Give the extent of all uninfected red blood cells.
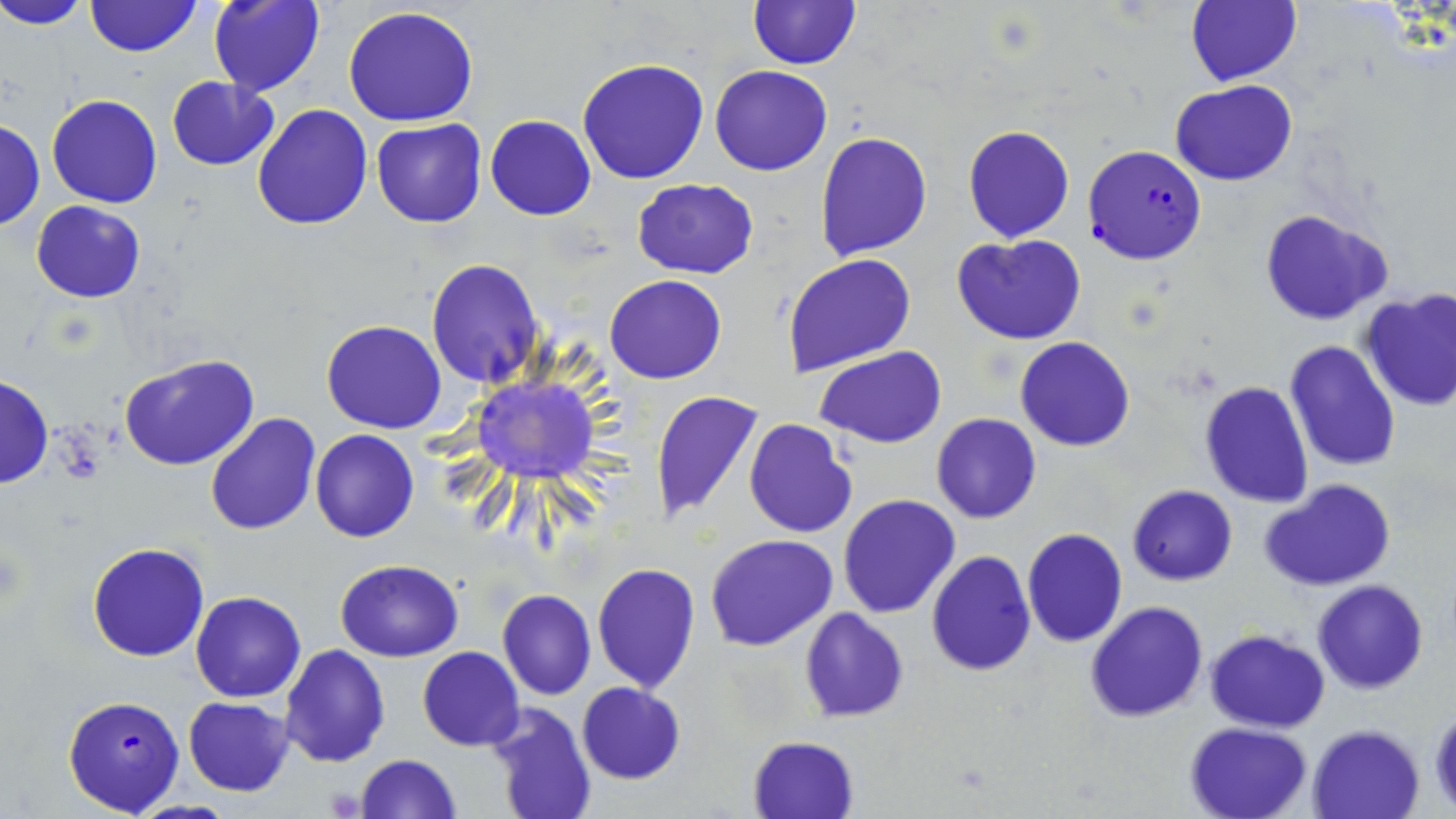

Approximate bounding boxes as named x1/y1/x2/y2 corners in pixels.
Uninfected red blood cells: (x1=0, y1=0, x2=91, y2=30), (x1=86, y1=0, x2=200, y2=56), (x1=208, y1=0, x2=325, y2=97), (x1=748, y1=0, x2=862, y2=70), (x1=1186, y1=0, x2=1301, y2=85), (x1=341, y1=7, x2=480, y2=128), (x1=576, y1=58, x2=709, y2=184), (x1=711, y1=65, x2=833, y2=176), (x1=167, y1=75, x2=279, y2=170), (x1=1170, y1=80, x2=1298, y2=184), (x1=47, y1=94, x2=161, y2=207), (x1=251, y1=102, x2=375, y2=230), (x1=485, y1=115, x2=597, y2=221), (x1=371, y1=118, x2=487, y2=227), (x1=0, y1=120, x2=45, y2=231), (x1=963, y1=125, x2=1074, y2=243), (x1=815, y1=130, x2=932, y2=261), (x1=632, y1=177, x2=759, y2=279), (x1=31, y1=200, x2=146, y2=302), (x1=1259, y1=208, x2=1392, y2=325), (x1=952, y1=233, x2=1087, y2=346), (x1=782, y1=253, x2=916, y2=376), (x1=425, y1=259, x2=544, y2=388), (x1=604, y1=274, x2=726, y2=384), (x1=1361, y1=288, x2=1456, y2=412), (x1=320, y1=319, x2=447, y2=433), (x1=1015, y1=336, x2=1135, y2=451), (x1=1284, y1=340, x2=1400, y2=470), (x1=816, y1=347, x2=947, y2=449), (x1=118, y1=354, x2=263, y2=473), (x1=1218, y1=369, x2=1399, y2=497), (x1=0, y1=375, x2=53, y2=489), (x1=472, y1=377, x2=599, y2=482), (x1=1198, y1=381, x2=1314, y2=509), (x1=651, y1=389, x2=765, y2=526), (x1=204, y1=414, x2=320, y2=535), (x1=931, y1=414, x2=1040, y2=523), (x1=743, y1=417, x2=858, y2=540), (x1=311, y1=429, x2=419, y2=542), (x1=1261, y1=479, x2=1396, y2=592), (x1=1128, y1=484, x2=1237, y2=585), (x1=837, y1=494, x2=960, y2=618), (x1=1021, y1=528, x2=1128, y2=648), (x1=706, y1=534, x2=839, y2=652), (x1=87, y1=542, x2=210, y2=662), (x1=925, y1=550, x2=1036, y2=676), (x1=334, y1=558, x2=464, y2=661), (x1=591, y1=562, x2=700, y2=693), (x1=1312, y1=579, x2=1429, y2=694), (x1=496, y1=589, x2=597, y2=699), (x1=191, y1=590, x2=306, y2=702), (x1=1085, y1=602, x2=1208, y2=722), (x1=798, y1=607, x2=909, y2=721), (x1=1205, y1=629, x2=1330, y2=731), (x1=280, y1=645, x2=391, y2=767), (x1=417, y1=646, x2=524, y2=749), (x1=576, y1=683, x2=685, y2=783), (x1=183, y1=696, x2=295, y2=795), (x1=485, y1=701, x2=597, y2=819), (x1=1429, y1=708, x2=1456, y2=813), (x1=1184, y1=722, x2=1313, y2=818), (x1=1309, y1=725, x2=1423, y2=819), (x1=747, y1=735, x2=858, y2=819), (x1=355, y1=753, x2=461, y2=818).

Summary:
  - Plasmodium falciparum-infected red blood cell locations: (x1=1083, y1=143, x2=1207, y2=266), (x1=62, y1=694, x2=185, y2=816)
  - Slide-level diagnosis: Plasmodium falciparum
  - Image size: 1456×819 pixels
  - Modality: optical microscopy
  - Preparation: thin blood smear
  - Field of view: one of a larger specimen
  - Magnification: 1000x
  - Stain: May-Grünwald-Giemsa